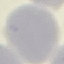
Summary:
  - Result: negative for malaria parasites
  - Capture: smartphone camera at the microscope eyepiece
  - Image type: cell patch, automatically extracted from a larger field of view and resized to 64 × 64 pixels
  - Preparation: thin smear
  - Stain: Giemsa